Comment on the morphology of the erythrocytes.
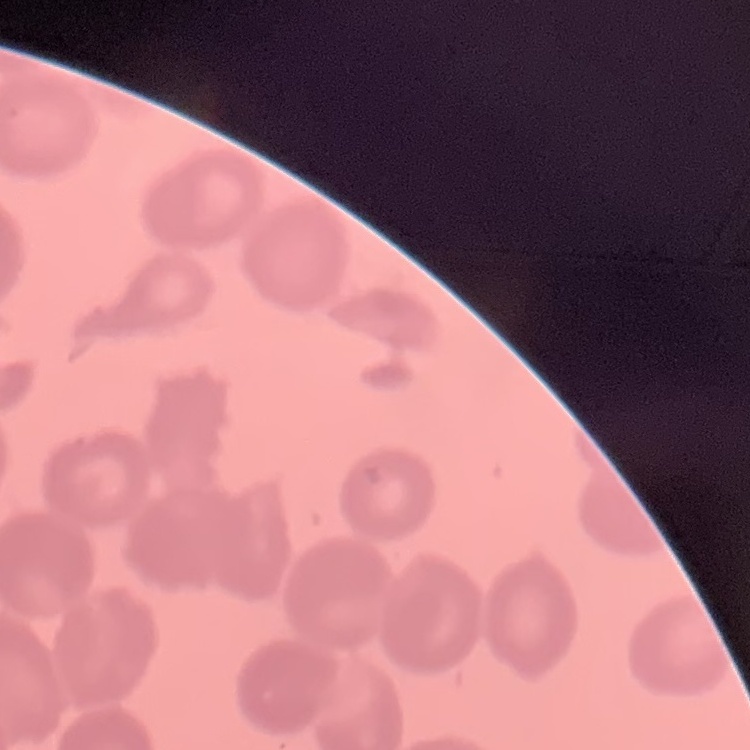

No rouleaux formation.

Stained with either Field's or Giemsa. Thin blood smear. Square crop of a larger photomicrograph.